Assess this cell for malaria.
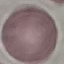
Uninfected.

capture = smartphone camera at the microscope eyepiece
stain = Giemsa
image type = automatically extracted cell patch, resized to 64 × 64 pixels
preparation = thin blood film